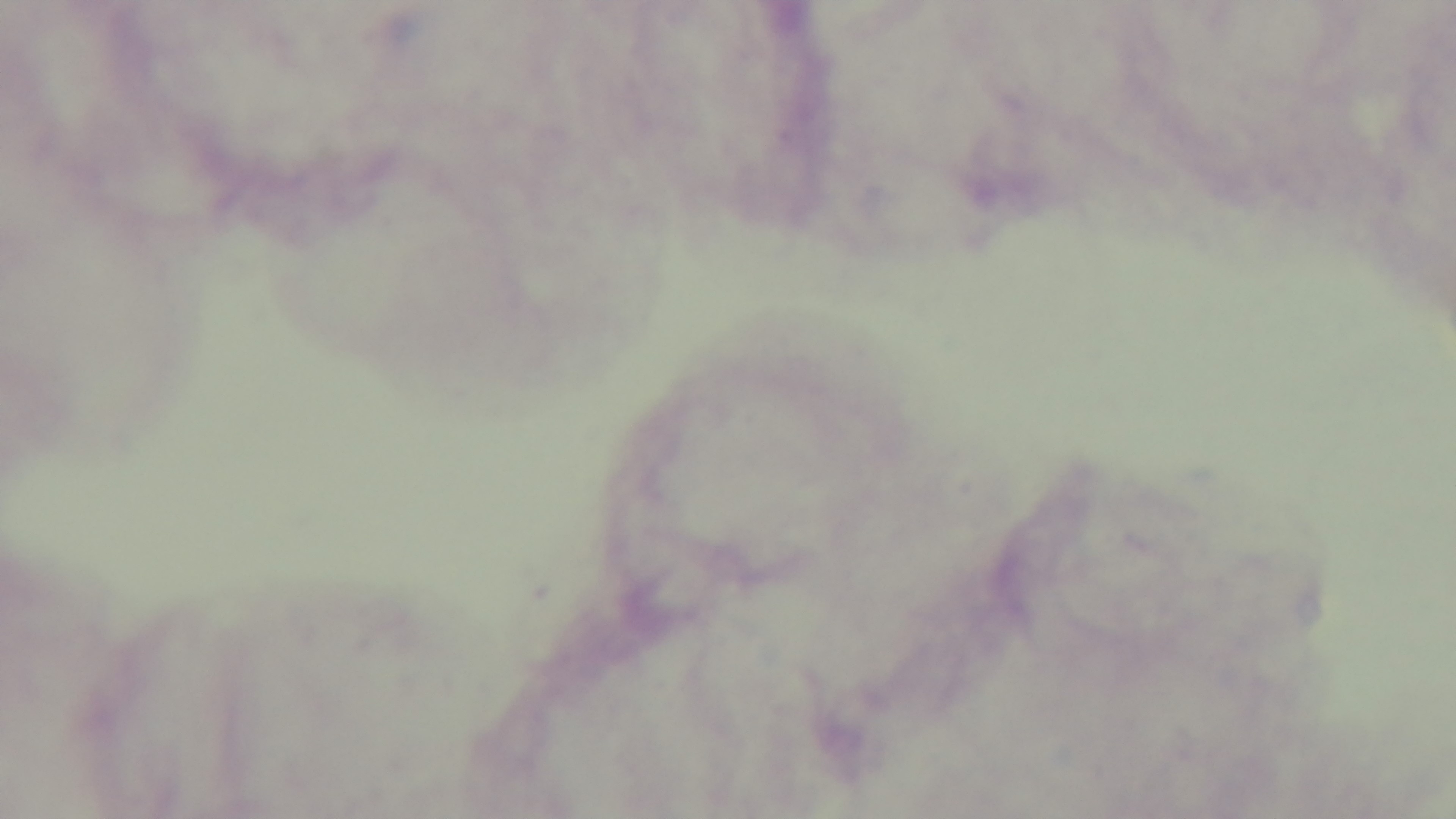
Photomicrograph. Captured with a mounted 4K digital camera. Preparation: thick blood film. 100x oil-immersion objective. Malaria status: uninfected. Single field of view. Giemsa-stained.